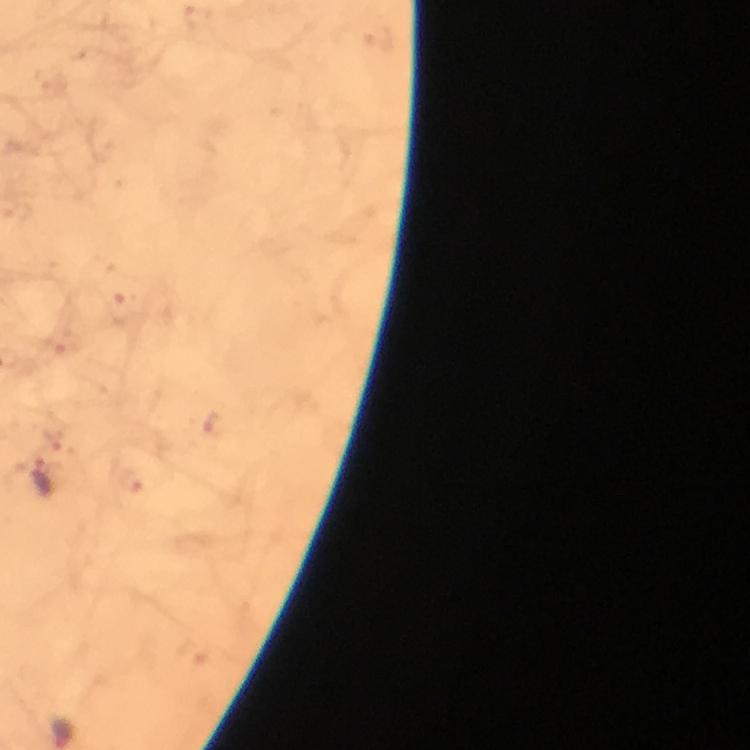
image_size: 750×750 pixels
malaria_parasite_locations: 'approximate centers as {x, y} in pixels: {216, 424}, {49, 475}'
magnification: 100x
immersion_oil: used
context: from a malaria diagnostic workup
capture: smartphone photograph through a microscope
preparation: thick blood film
cropped_from: a single field of view
stain: Giemsa